Identify the blood parasite species.
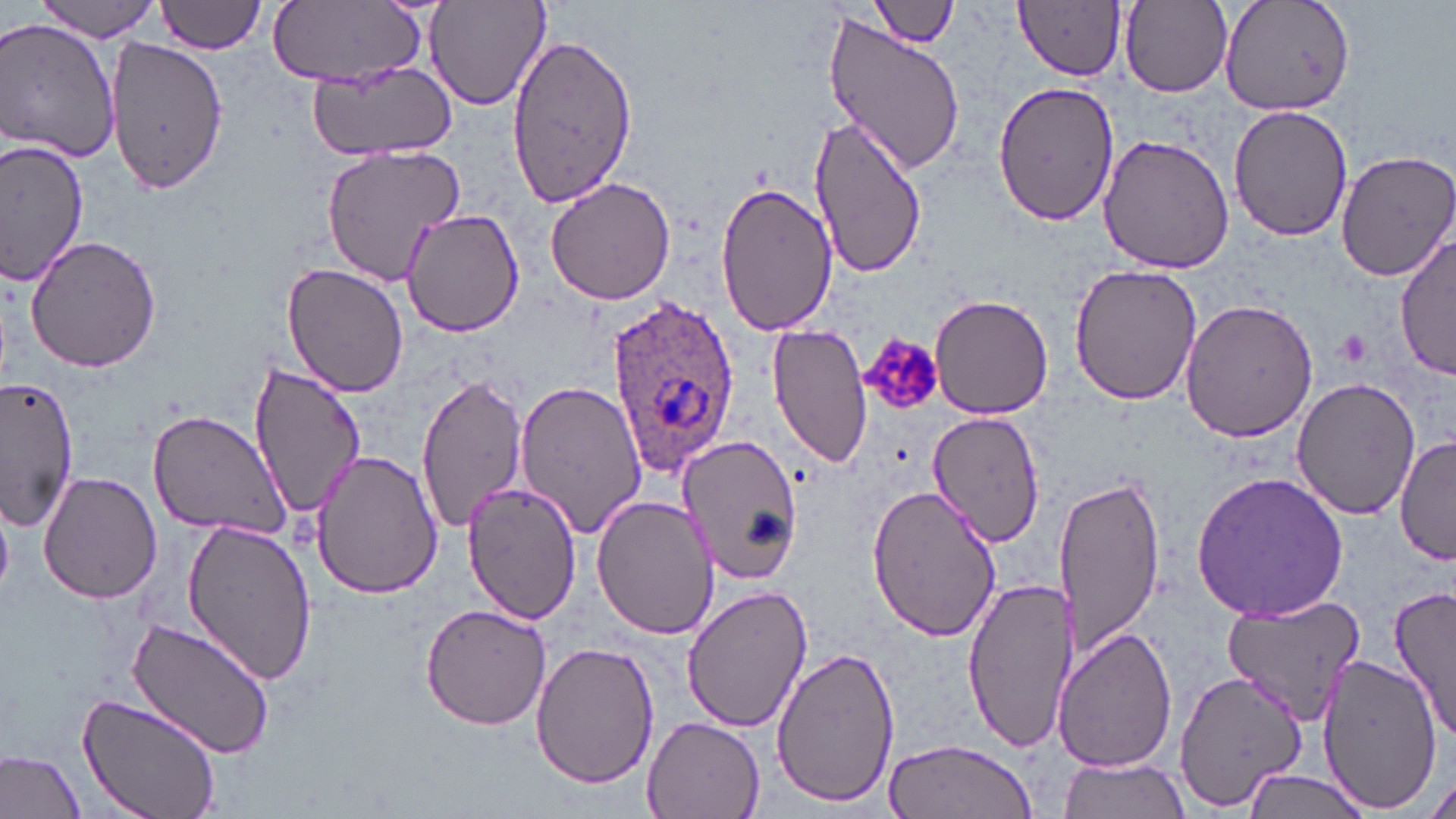
Plasmodium ovale.

stain = May-Grünwald-Giemsa
uninfected red blood cell locations = approximate bounding boxes as (x1, y1, x2, y2) in pixels: (158, 0, 267, 54), (424, 0, 551, 112), (872, 0, 959, 47), (1016, 0, 1126, 80), (1218, 0, 1357, 116), (31, 1, 167, 40), (1120, 1, 1232, 96), (268, 2, 425, 86), (820, 14, 969, 175), (0, 18, 120, 164), (504, 30, 637, 211), (107, 36, 228, 195), (308, 61, 459, 163), (993, 80, 1120, 227), (1229, 103, 1352, 243), (810, 120, 924, 277), (1097, 135, 1234, 273), (0, 141, 88, 285), (320, 144, 468, 288), (1335, 149, 1456, 283), (546, 174, 679, 306), (714, 183, 839, 338), (401, 209, 525, 337), (1396, 233, 1455, 383), (25, 234, 162, 374), (280, 261, 410, 398), (1067, 261, 1205, 404), (928, 295, 1055, 419), (1179, 297, 1318, 442), (768, 323, 874, 469), (245, 358, 365, 520), (415, 370, 528, 536), (3, 373, 80, 531), (514, 377, 646, 541), (1291, 379, 1420, 519), (925, 409, 1048, 549), (148, 410, 291, 539), (678, 434, 805, 586), (1394, 436, 1455, 564), (308, 447, 443, 601), (1052, 469, 1167, 657), (38, 471, 162, 605), (1190, 471, 1352, 623), (864, 480, 1004, 643), (460, 481, 583, 624), (592, 494, 718, 640), (0, 499, 13, 595), (181, 517, 320, 685), (961, 573, 1079, 754), (682, 585, 813, 735), (1390, 586, 1456, 740), (1221, 596, 1369, 721), (420, 603, 552, 730), (128, 618, 276, 762), (1054, 628, 1178, 772), (531, 641, 659, 789), (769, 644, 898, 807), (1316, 653, 1441, 814), (1173, 668, 1311, 810), (77, 694, 221, 818), (641, 714, 765, 819), (882, 738, 1035, 818), (0, 748, 86, 818), (1055, 754, 1190, 819), (1239, 770, 1375, 819), (1423, 775, 1456, 819)
image size = 1456×819 pixels
platelet locations = approximate bounding boxes as (x1, y1, x2, y2) in pixels: (863, 333, 942, 409)
Plasmodium ovale-infected red blood cell locations = approximate bounding boxes as (x1, y1, x2, y2) in pixels: (607, 294, 741, 476)
preparation = thin blood smear
magnification = 1000x
field of view = single
modality = light microscopy